Assess this cell for malaria.
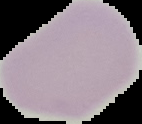

It is uninfected.

Image is 142×124 pixels. Segmented cell region on a black background. From a thin blood smear.